Point out each Plasmodium parasite.
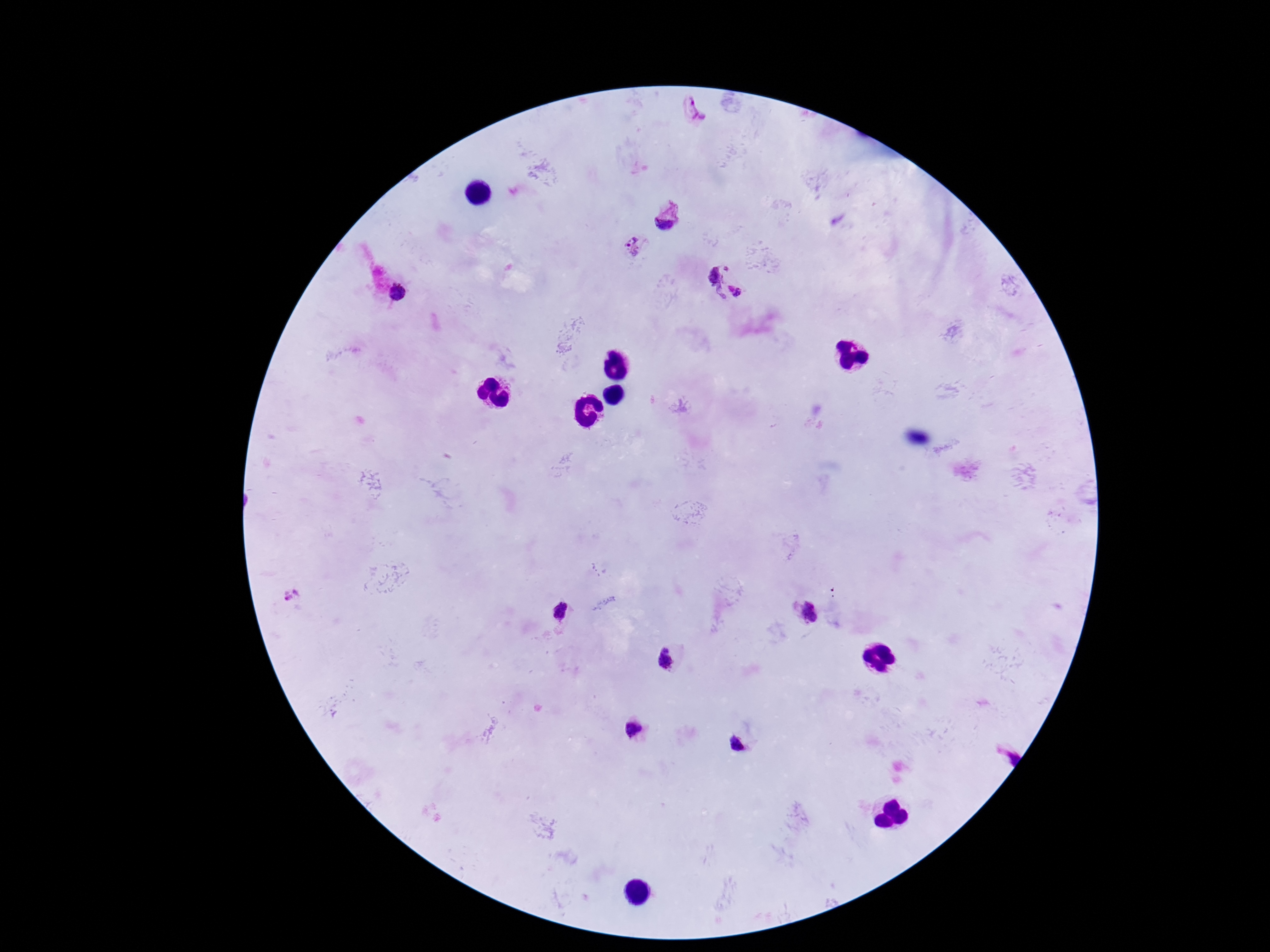
Approximate object centers, in pixels from the top-left corner.
Plasmodium parasites: (x=695, y=112), (x=668, y=218), (x=636, y=245), (x=728, y=266), (x=718, y=283), (x=398, y=291), (x=736, y=291), (x=292, y=595), (x=806, y=609), (x=559, y=611), (x=666, y=659), (x=632, y=728), (x=738, y=742), (x=1002, y=751).

stain = Giemsa
capture = smartphone camera through the microscope eyepiece
patient malaria status = infected
magnification = 100x
preparation = thick blood film
image size = 1270×952 pixels
field of view = single